Assess the morphology of the red blood cells.
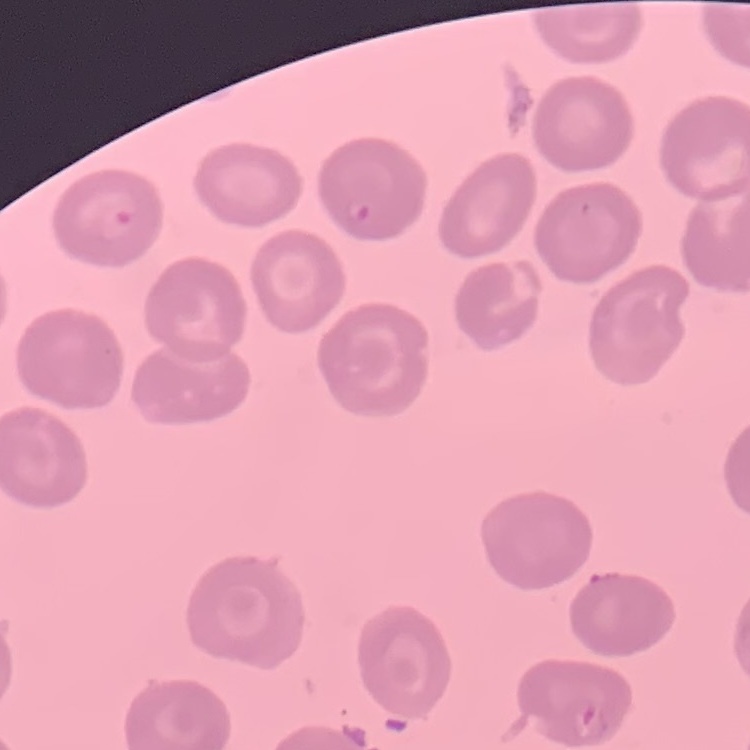
They show no rouleaux formation.

One tile cut from a larger photomicrograph. Thin blood film. Field's or Giemsa stain.